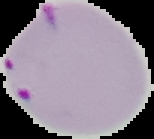
From a thin blood film. Result: Plasmodium parasites identified. Image is 154×139 pixels. Segmented cell region on a black background.